Give the position of every Plasmodium parasite visible.
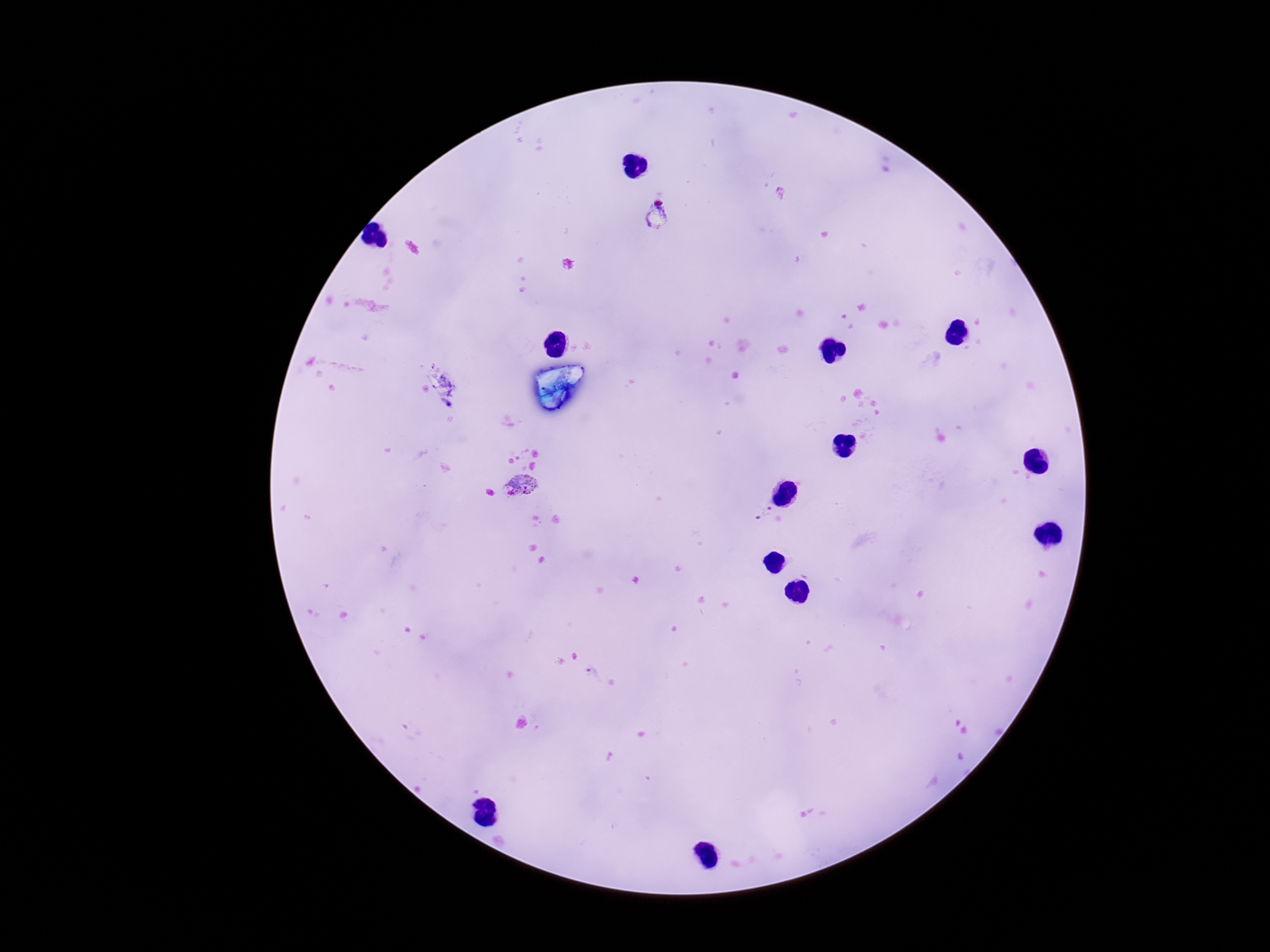

Approximate object centers, in pixels from the top-left corner.
Plasmodium parasites: (x=521, y=485), (x=763, y=513), (x=592, y=673).

Image is 1270×952 pixels. Thick blood smear. 100x magnification. Patient malaria status: positive. Giemsa-stained preparation. Smartphone photograph taken through the microscope eyepiece. One field from this slide.